Assess this cell for malaria.
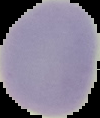
It is uninfected.

Summary:
  - Image size: 100×118 pixels
  - Image type: segmented cell region with the area outside set to black
  - Preparation: thin blood smear